Comment on the morphology of the erythrocytes.
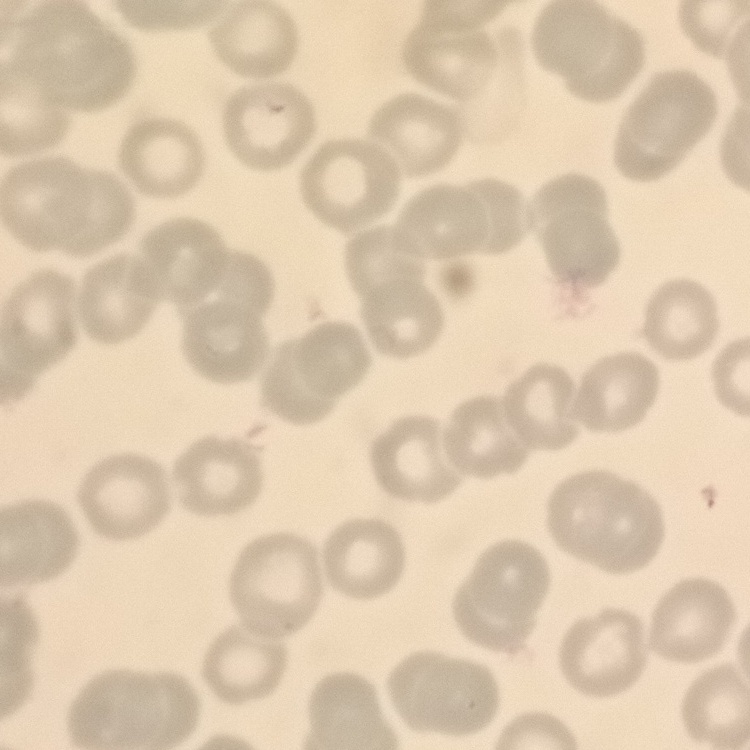
They show no rouleaux formation.

{
  "image_type": "one tile cut from a larger photomicrograph",
  "preparation": "thin peripheral smear",
  "stain": "Field's or Giemsa"
}